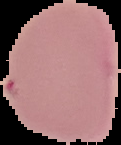

preparation = thin blood film
image size = 121×145 pixels
malaria status = uninfected
image type = segmented cell region with the area outside set to black